Classify this cell by malaria status.
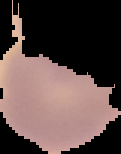

Uninfected.

Image is 121×154 pixels. The area outside the segmented cell region is set to black. From a thin blood film.